Describe the morphology of the erythrocytes.
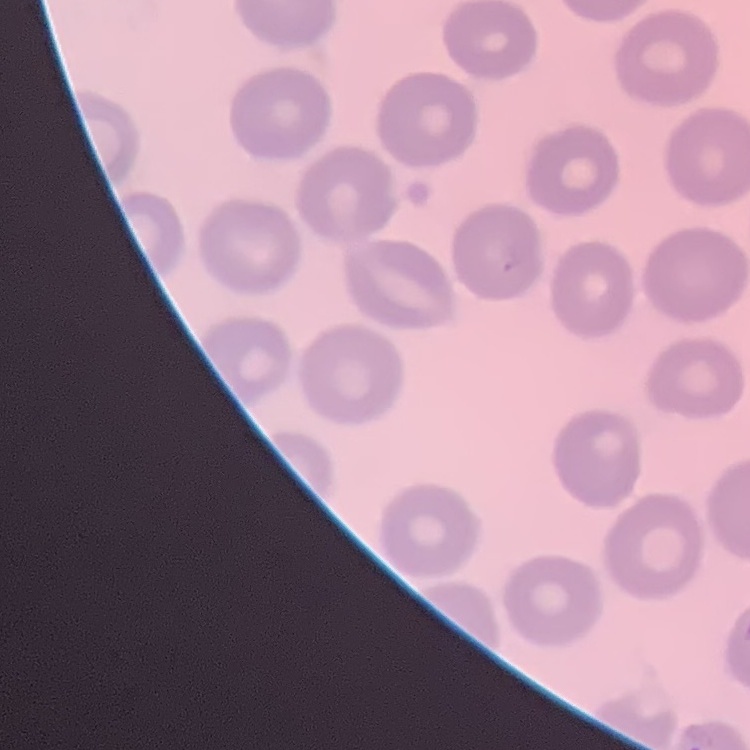
They show no rouleaux formation.

Summary:
  - Image type: one tile cut from a larger photomicrograph
  - Stain: Field's or Giemsa
  - Preparation: thin blood smear